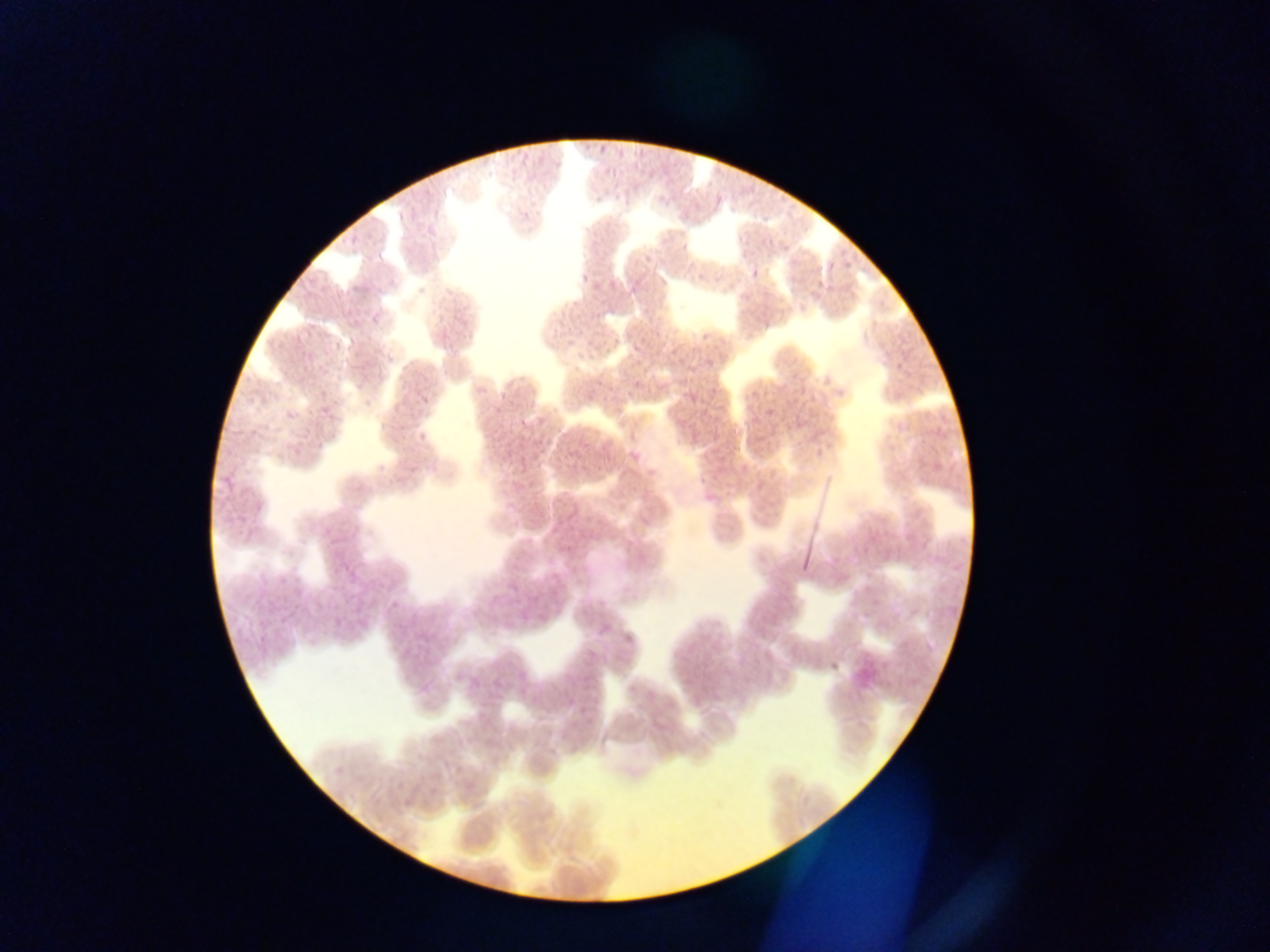

Approximate bounding boxes as {left, top, right, bottom} in pixels.
Summary:
  - Plasmodium parasite locations: {759, 235, 775, 249}, {344, 236, 359, 247}, {776, 244, 792, 252}, {836, 248, 852, 274}, {636, 252, 652, 266}, {818, 257, 836, 271}, {746, 263, 762, 278}, {576, 270, 590, 288}, {348, 277, 362, 293}, {623, 278, 643, 304}, {807, 281, 822, 300}, {371, 314, 380, 326}, {863, 317, 886, 336}, {696, 321, 711, 342}, {302, 326, 320, 344}, {277, 330, 294, 348}, {327, 339, 338, 354}, {628, 339, 645, 353}, {383, 344, 397, 364}, {667, 346, 683, 358}, {894, 347, 909, 376}, {629, 377, 649, 388}, {354, 380, 365, 390}, {583, 384, 596, 400}, {413, 392, 429, 408}, {685, 392, 696, 403}, {490, 397, 504, 418}, {762, 397, 784, 417}, {302, 404, 316, 417}, {282, 408, 294, 421}, {708, 410, 724, 435}, {515, 413, 532, 427}, {676, 416, 690, 426}, {930, 419, 943, 444}, {249, 421, 260, 439}, {628, 429, 642, 440}, {415, 433, 426, 443}, {562, 437, 583, 462}, {515, 450, 534, 470}, {714, 450, 732, 472}, {627, 452, 638, 463}, {375, 457, 385, 472}, {216, 467, 238, 499}, {703, 487, 719, 503}, {561, 510, 581, 523}, {345, 567, 362, 584}, {274, 579, 292, 604}, {387, 598, 406, 612}, {533, 611, 545, 622}, {510, 613, 521, 631}, {597, 614, 614, 641}, {331, 615, 342, 629}, {356, 616, 367, 627}
  - Field of view: single
  - Country: Ghana
  - Capture: mobile-phone photograph through a microscope
  - Image size: 1270×952 pixels
  - Preparation: thin blood film